Comment on the morphology of the red blood cells.
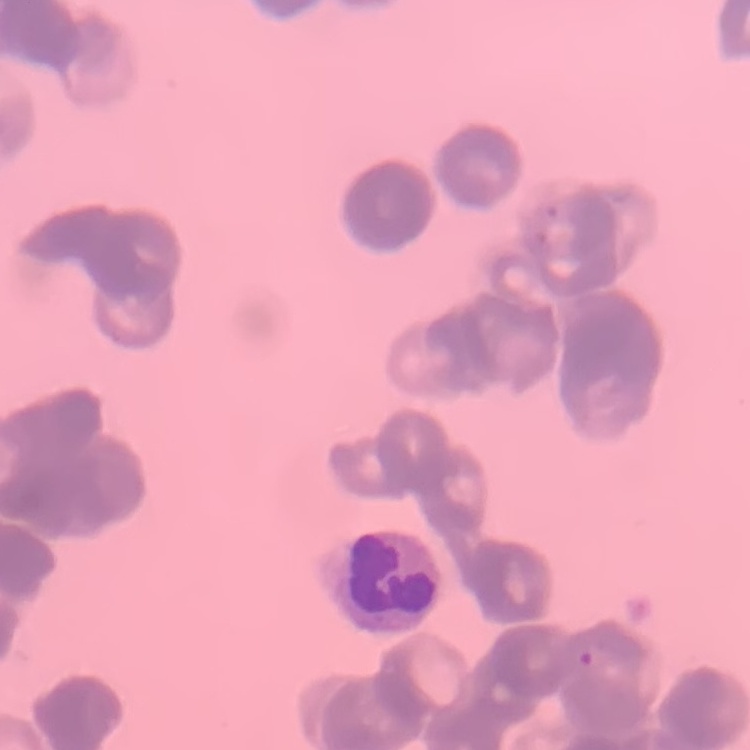
They show rouleaux formation.

Summary:
  - Preparation: thin blood film
  - Stain: Field's or Giemsa
  - Image type: one tile cut from a larger photomicrograph